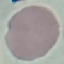

Summary:
  - Malaria status: uninfected
  - Preparation: thin blood film
  - Image type: cell patch, automatically extracted from a larger field of view and resized to 64 × 64 pixels
  - Stain: Giemsa
  - Capture: smartphone through the microscope eyepiece